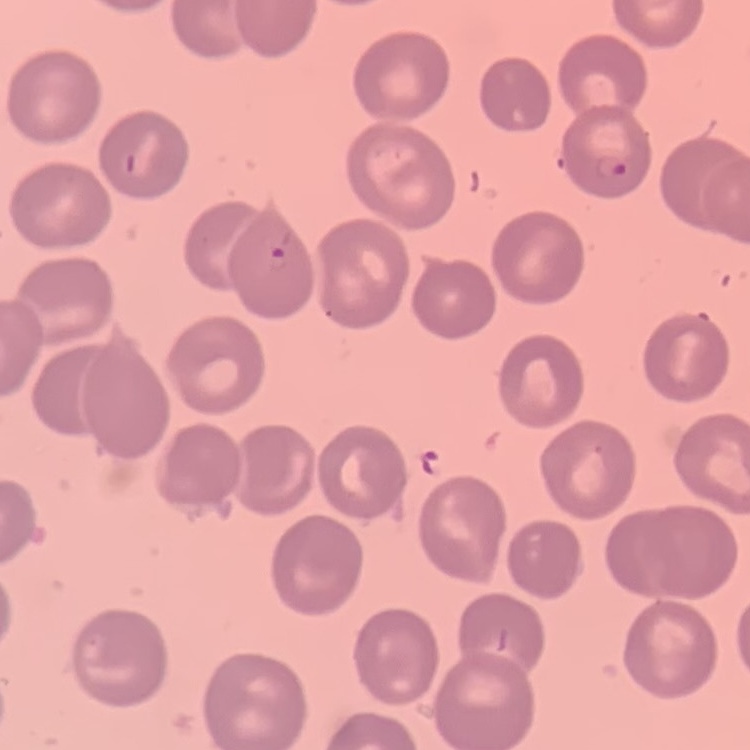

red blood cell morphology = no rouleaux formation
image type = one tile cut from a larger photomicrograph
stain = Field's or Giemsa
preparation = thin blood film